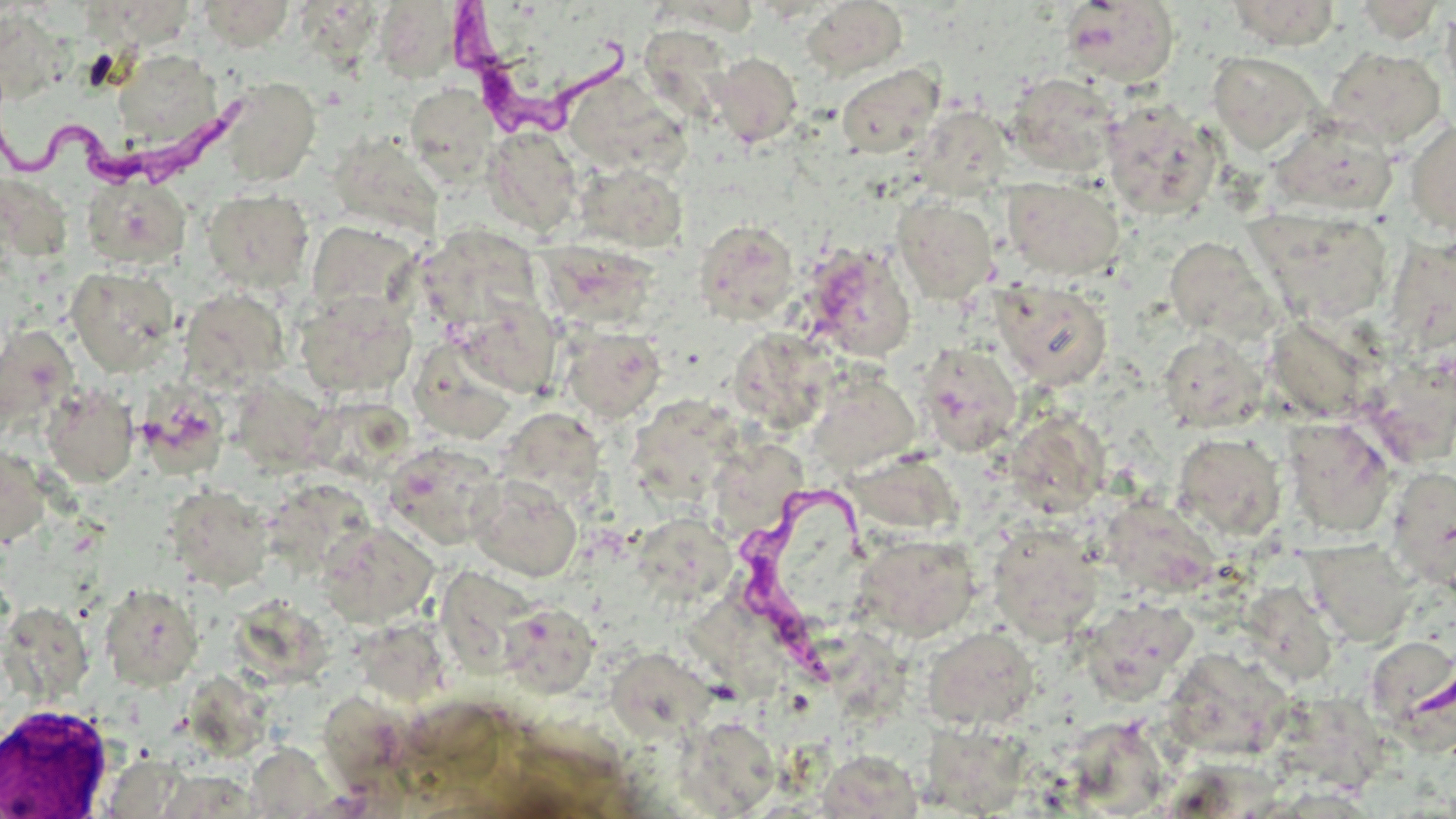
Summary:
  - Coordinate format: approximate bounding boxes as named x1/y1/x2/y2 corners in pixels
  - White blood cell locations: (x1=0, y1=703, x2=114, y2=817)
  - Trypanosoma brucei locations: (x1=450, y1=6, x2=634, y2=141), (x1=1, y1=86, x2=249, y2=195), (x1=733, y1=476, x2=898, y2=683)
  - Uninfected red blood cell locations: (x1=199, y1=0, x2=295, y2=51), (x1=1226, y1=0, x2=1341, y2=49), (x1=801, y1=1, x2=908, y2=79), (x1=1060, y1=1, x2=1179, y2=87), (x1=1351, y1=1, x2=1446, y2=43), (x1=374, y1=3, x2=462, y2=81), (x1=92, y1=5, x2=193, y2=44), (x1=1441, y1=6, x2=1456, y2=100), (x1=0, y1=9, x2=70, y2=104), (x1=638, y1=24, x2=736, y2=122), (x1=1324, y1=46, x2=1446, y2=147), (x1=113, y1=48, x2=225, y2=148), (x1=1207, y1=51, x2=1323, y2=153), (x1=710, y1=52, x2=802, y2=147), (x1=836, y1=64, x2=944, y2=158), (x1=1006, y1=72, x2=1122, y2=177), (x1=215, y1=77, x2=321, y2=187), (x1=576, y1=80, x2=701, y2=182), (x1=405, y1=84, x2=499, y2=185), (x1=1101, y1=99, x2=1220, y2=218), (x1=914, y1=107, x2=1013, y2=199), (x1=1268, y1=116, x2=1397, y2=217), (x1=1405, y1=119, x2=1456, y2=236), (x1=484, y1=127, x2=583, y2=236), (x1=329, y1=133, x2=442, y2=237), (x1=575, y1=162, x2=688, y2=252), (x1=3, y1=175, x2=71, y2=257), (x1=82, y1=175, x2=191, y2=270), (x1=1002, y1=176, x2=1124, y2=281), (x1=201, y1=188, x2=315, y2=293), (x1=892, y1=197, x2=998, y2=304), (x1=1250, y1=208, x2=1394, y2=325), (x1=701, y1=219, x2=799, y2=321), (x1=306, y1=221, x2=419, y2=320), (x1=416, y1=225, x2=544, y2=333), (x1=1164, y1=237, x2=1277, y2=342), (x1=538, y1=240, x2=660, y2=332), (x1=801, y1=243, x2=917, y2=362), (x1=65, y1=266, x2=179, y2=375), (x1=991, y1=279, x2=1112, y2=389), (x1=180, y1=287, x2=291, y2=392), (x1=295, y1=290, x2=417, y2=399), (x1=452, y1=295, x2=562, y2=399), (x1=0, y1=325, x2=77, y2=429), (x1=559, y1=325, x2=667, y2=422), (x1=1157, y1=331, x2=1266, y2=432), (x1=741, y1=338, x2=839, y2=434), (x1=915, y1=343, x2=1022, y2=456), (x1=420, y1=352, x2=512, y2=447), (x1=1359, y1=353, x2=1456, y2=466), (x1=807, y1=376, x2=920, y2=476), (x1=229, y1=378, x2=332, y2=473), (x1=41, y1=384, x2=139, y2=487), (x1=136, y1=385, x2=230, y2=477), (x1=630, y1=400, x2=743, y2=507), (x1=1008, y1=400, x2=1109, y2=521), (x1=500, y1=407, x2=607, y2=504), (x1=1283, y1=418, x2=1395, y2=537), (x1=1172, y1=433, x2=1286, y2=540), (x1=715, y1=436, x2=803, y2=526), (x1=384, y1=442, x2=502, y2=548), (x1=0, y1=443, x2=51, y2=551), (x1=1386, y1=466, x2=1456, y2=589), (x1=467, y1=474, x2=582, y2=582), (x1=164, y1=485, x2=274, y2=592), (x1=275, y1=491, x2=375, y2=573), (x1=1118, y1=503, x2=1215, y2=593), (x1=318, y1=520, x2=439, y2=628), (x1=987, y1=522, x2=1104, y2=643), (x1=639, y1=530, x2=736, y2=608), (x1=853, y1=533, x2=980, y2=642), (x1=1302, y1=539, x2=1416, y2=646), (x1=433, y1=562, x2=552, y2=678), (x1=1243, y1=578, x2=1331, y2=683), (x1=99, y1=582, x2=204, y2=690), (x1=686, y1=592, x2=783, y2=707), (x1=1079, y1=596, x2=1199, y2=701), (x1=499, y1=603, x2=600, y2=698), (x1=237, y1=604, x2=332, y2=694), (x1=0, y1=606, x2=102, y2=708), (x1=361, y1=623, x2=450, y2=698), (x1=921, y1=626, x2=1039, y2=731), (x1=835, y1=640, x2=908, y2=722), (x1=606, y1=647, x2=715, y2=743), (x1=1365, y1=647, x2=1455, y2=761), (x1=1172, y1=660, x2=1288, y2=762), (x1=196, y1=683, x2=290, y2=759), (x1=315, y1=687, x2=405, y2=781), (x1=1296, y1=694, x2=1388, y2=788), (x1=679, y1=715, x2=781, y2=815), (x1=1066, y1=722, x2=1160, y2=808), (x1=937, y1=742, x2=1032, y2=818), (x1=822, y1=753, x2=929, y2=813), (x1=157, y1=770, x2=261, y2=817)
  - Slide-level diagnosis: Trypanosoma brucei
  - Modality: optical microscopy
  - Magnification: 1000x
  - Preparation: thin blood film
  - Stain: May-Grünwald-Giemsa
  - Field of view: one of a larger specimen
  - Image size: 1456×819 pixels